Describe the morphology of the erythrocytes.
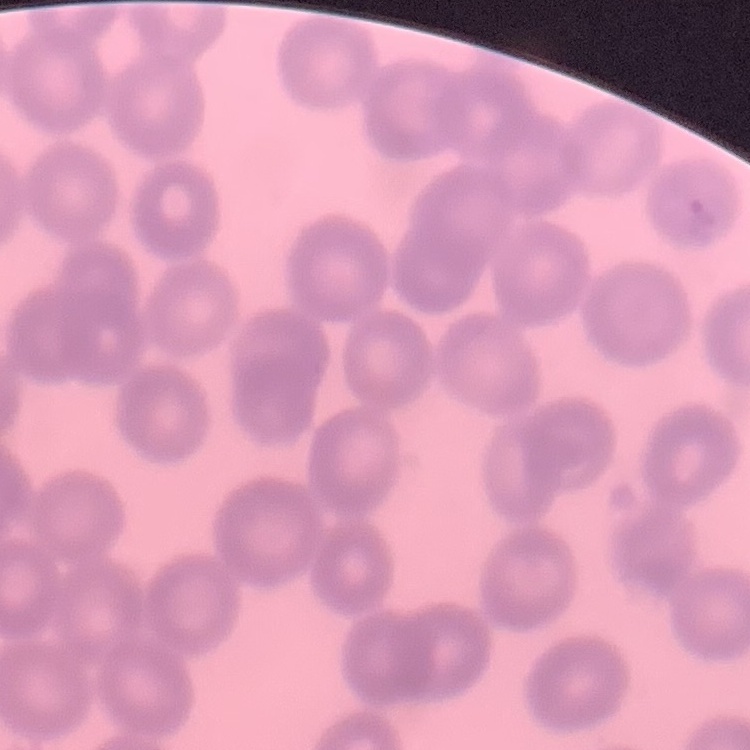
They show no rouleaux formation.

Thin blood film. Square crop of a larger photomicrograph. Stained with either Field's or Giemsa.